Identify the parasite.
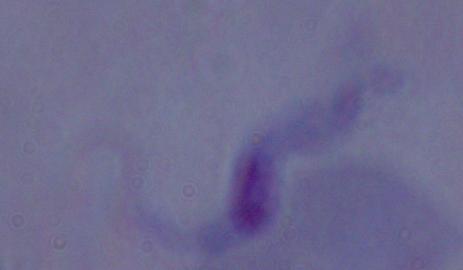
A trypanosome.

Summary:
  - Magnification: 1000x
  - Modality: micrograph